Classify this cell by malaria status.
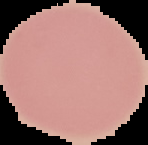

Uninfected.

The area outside the segmented cell region is set to black. Image is 148×145 pixels. From a thin blood smear.